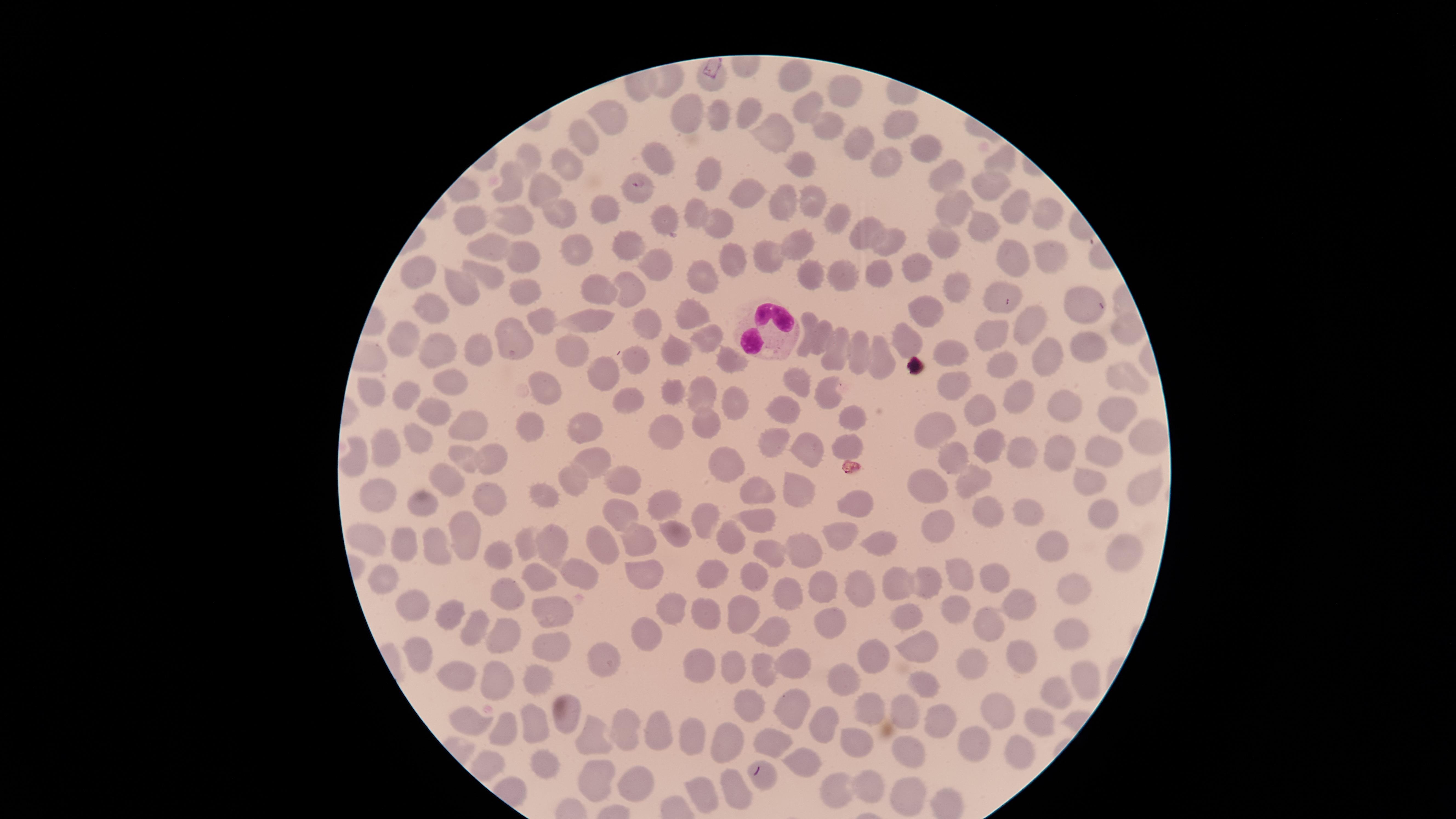

Approximate marker points as (x, y) in pixels. White blood cells: (762, 329). Uninfected red blood cells: (797, 67), (840, 88), (804, 106), (687, 110), (750, 112), (607, 116), (721, 116), (823, 122), (894, 123), (589, 131), (775, 138), (862, 139), (927, 145), (529, 154), (881, 159), (1004, 159), (668, 161), (804, 163), (563, 166), (713, 174), (941, 176), (991, 179), (512, 186), (542, 187), (755, 194), (643, 196), (784, 199), (814, 199), (1016, 204), (951, 207), (603, 209), (840, 211), (1049, 211), (698, 212), (468, 213), (559, 214), (663, 214), (512, 216), (719, 226), (988, 226), (870, 233), (894, 239), (633, 242), (798, 245), (947, 246), (494, 247), (582, 249), (1046, 250), (771, 251), (523, 257), (736, 259), (1015, 259), (660, 261), (917, 265), (425, 272), (490, 274), (812, 274), (844, 276), (882, 278), (463, 283), (706, 283), (997, 285), (528, 286), (636, 286), (954, 287), (604, 289), (1085, 302), (434, 306), (925, 308), (695, 312), (543, 318), (591, 324), (650, 324), (1030, 327), (1120, 330), (995, 331), (821, 333), (706, 334), (811, 334), (394, 336), (517, 336), (909, 339), (475, 345), (1092, 346), (440, 348), (838, 348), (956, 349), (571, 351), (673, 351), (728, 355), (861, 357), (1046, 357), (878, 359), (642, 363), (1004, 363), (608, 377), (451, 378), (799, 378), (1118, 381), (954, 382), (546, 384), (673, 390), (709, 393), (729, 395), (829, 395), (370, 396), (402, 398), (1017, 399), (434, 402), (631, 403), (1066, 409), (786, 411), (985, 411), (1113, 413), (588, 416), (527, 418), (465, 419), (851, 421), (666, 425), (707, 426), (932, 426), (419, 432), (781, 435), (1143, 439), (809, 442), (955, 443), (1059, 445), (386, 446), (853, 448), (991, 448), (1022, 451), (1102, 452), (462, 455), (593, 456), (489, 459), (357, 463), (722, 464), (971, 473), (572, 475), (623, 477), (453, 479), (929, 481), (1145, 482), (757, 485), (1097, 487), (377, 490), (489, 493), (545, 493), (802, 494), (674, 497), (856, 501), (422, 506), (1027, 506), (986, 508), (620, 510), (1104, 510), (704, 512), (757, 518), (935, 521), (467, 526), (674, 533), (839, 533), (370, 538), (435, 538), (523, 538), (552, 539), (634, 539), (881, 539), (730, 540), (405, 543), (607, 545), (802, 545), (1053, 549), (772, 550), (1123, 552), (507, 556), (960, 569), (574, 571), (640, 571), (712, 572), (758, 575), (535, 576), (896, 577), (991, 577), (820, 580), (856, 581), (929, 581), (384, 584), (1077, 585), (785, 590), (408, 598), (504, 600), (556, 601), (1012, 601), (954, 606), (672, 608), (706, 610), (450, 611), (746, 612), (906, 620), (992, 621), (833, 625), (470, 626), (1076, 626), (768, 630), (506, 631), (643, 635), (547, 641), (918, 644), (1017, 645), (416, 649), (869, 653), (611, 658), (788, 661), (703, 664), (973, 667), (459, 669), (734, 671), (766, 671), (1080, 674), (844, 677), (536, 680), (929, 681), (498, 686), (1054, 694), (742, 705), (786, 707), (872, 709), (993, 711), (906, 712), (529, 719), (566, 719), (938, 719), (470, 721), (823, 723), (1039, 725), (504, 728), (623, 728), (658, 729), (693, 738), (594, 739), (776, 741), (727, 743), (855, 743), (973, 744), (907, 749), (1017, 757), (808, 765), (542, 766), (598, 776), (766, 777), (867, 782), (633, 785), (704, 790), (735, 790), (906, 792), (843, 793). Presence: no malaria parasites detected. Thin blood film. Giemsa-stained preparation. Smartphone photograph through the microscope eyepiece. Circular visible region. Single field of view. Image is 1456×819 pixels.